Give the position of every malaria parasite.
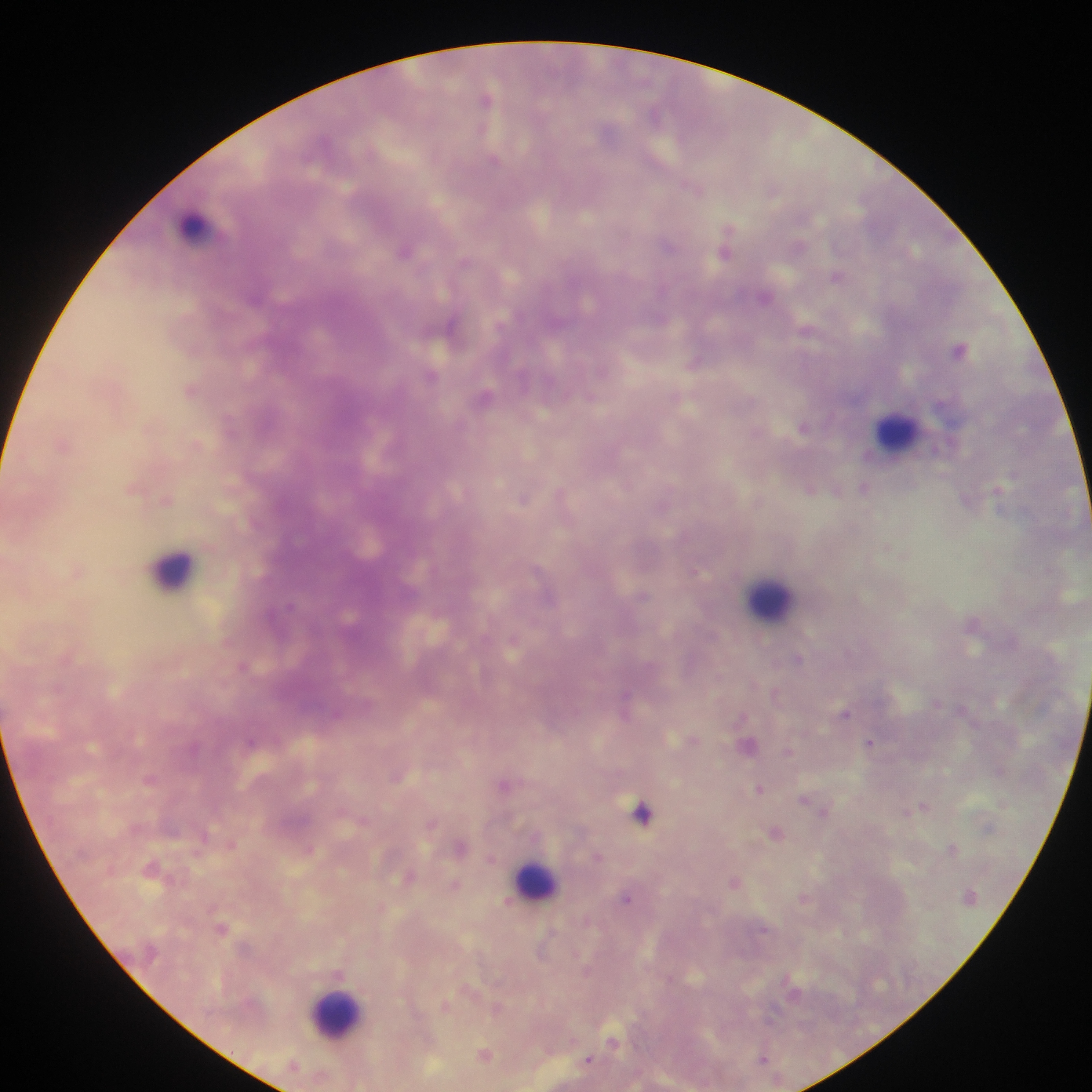

Approximate centers as (x, y) in pixels.
Malaria parasites: (487, 98), (655, 113), (494, 160), (693, 187), (669, 245), (405, 249), (726, 249), (838, 275), (765, 296), (453, 326), (809, 329), (960, 348), (696, 362), (432, 376), (191, 390), (486, 396), (591, 397), (229, 424), (803, 427), (64, 444), (197, 444), (134, 488), (865, 488), (811, 489), (838, 491), (999, 491), (562, 495), (523, 498), (166, 499), (967, 500), (78, 569), (698, 571), (641, 596), (974, 624), (513, 642), (798, 660), (243, 666), (776, 693), (937, 703), (626, 704), (845, 712), (336, 714), (742, 716), (694, 740), (252, 743), (871, 743), (749, 746), (789, 750), (150, 778), (506, 784), (760, 788), (805, 800), (813, 804), (924, 806), (824, 811), (642, 812), (364, 820), (433, 824), (775, 831), (232, 844), (461, 845), (309, 849), (952, 849), (597, 856), (491, 859), (153, 868), (409, 876), (735, 883), (455, 885), (627, 898), (805, 898), (222, 928), (765, 930), (587, 971), (793, 988), (447, 1005), (497, 1008), (614, 1041), (485, 1054), (763, 1058), (589, 1059).

Summary:
  - Leukocyte locations: (194, 225), (896, 432), (171, 569), (771, 599), (536, 881), (335, 1014)
  - Country: Ghana
  - Image size: 1092×1092 pixels
  - Field of view: single
  - Preparation: thick blood film
  - Capture: mobile-phone photograph through a microscope